Describe the morphology of the red blood cells.
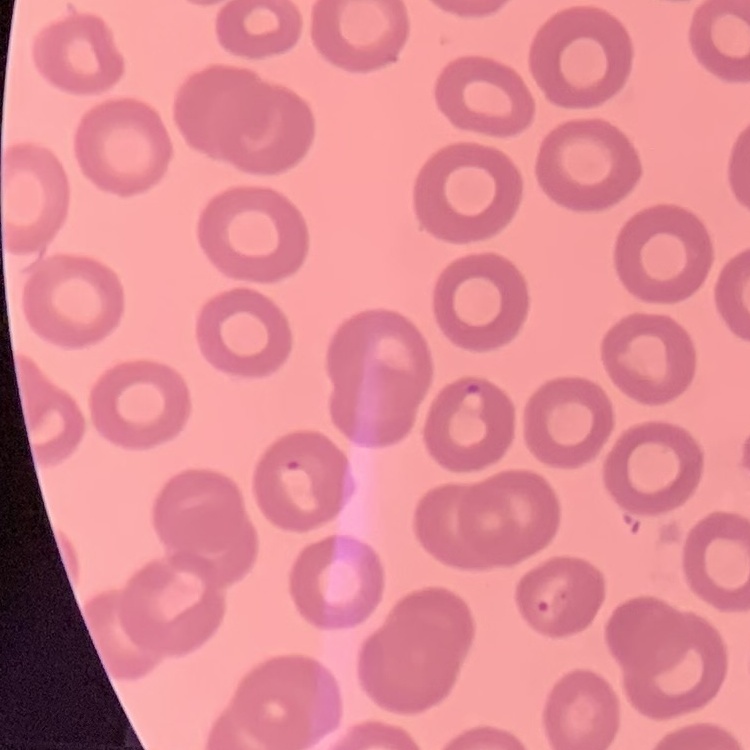
No rouleaux formation.

{
  "preparation": "thin blood smear",
  "stain": "Field's or Giemsa",
  "image_type": "square crop of a larger photomicrograph"
}